Locate every Plasmodium ovale-infected red blood cell.
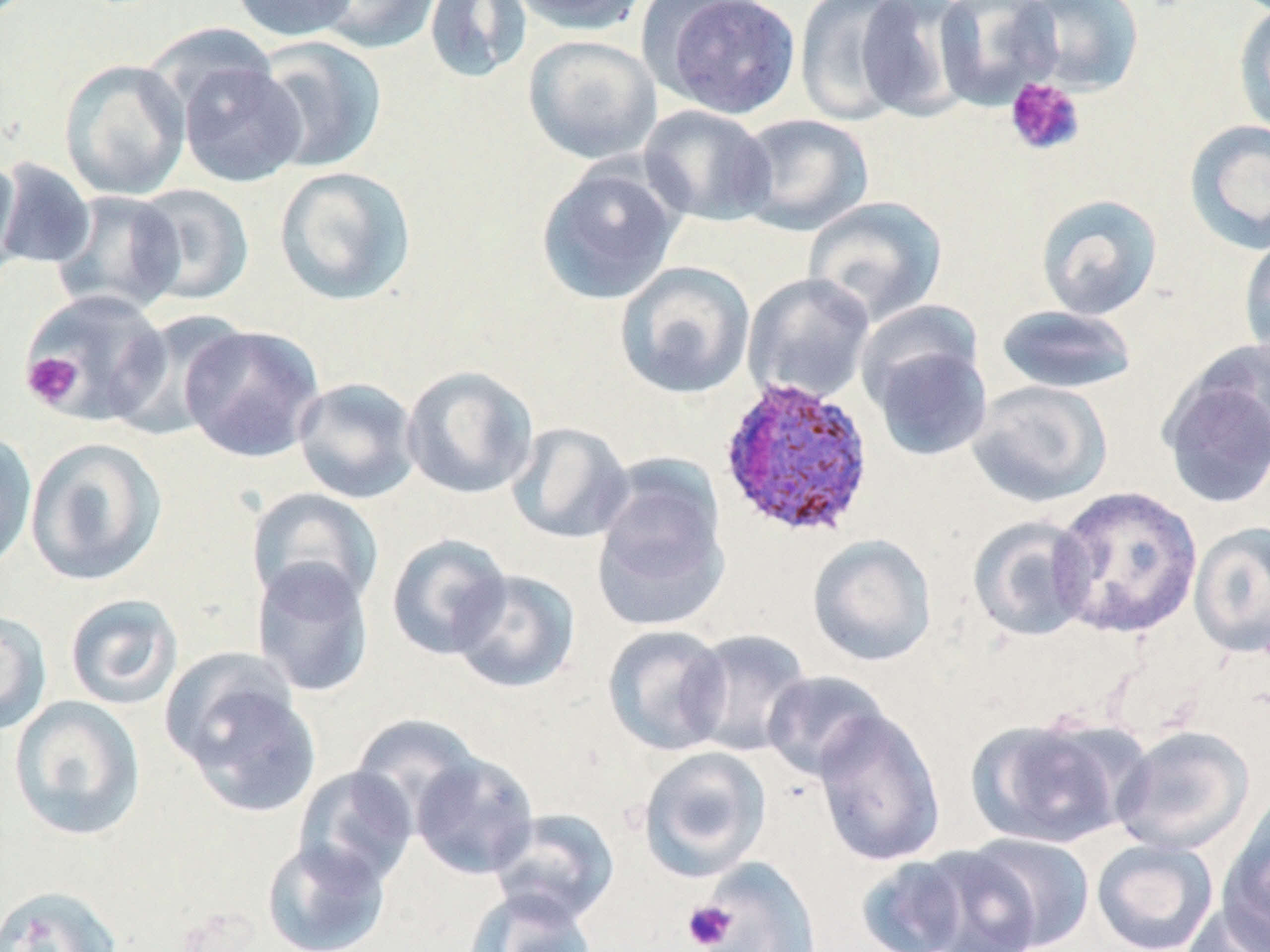

Approximate bounding boxes as (x1, y1, x2, y2) in pixels.
Plasmodium ovale-infected red blood cells: (718, 375, 876, 541).

{
  "slide_level_diagnosis": "Plasmodium ovale",
  "image_size": "1270×952 pixels",
  "preparation": "thin blood smear",
  "platelet_locations": "approximate bounding boxes as (x1, y1, x2, y2) in pixels: (1004, 77, 1086, 157), (22, 351, 83, 409), (682, 900, 737, 950)",
  "magnification": "1000x",
  "stain": "May-Grünwald-Giemsa",
  "modality": "light microscopy",
  "field_of_view": "one of a larger specimen",
  "uninfected_red_blood_cell_locations": "approximate bounding boxes as (x1, y1, x2, y2) in pixels: (230, 0, 359, 42), (311, 0, 441, 54), (423, 0, 532, 84), (507, 0, 650, 34), (649, 0, 802, 119), (794, 0, 920, 126), (854, 0, 974, 121), (933, 0, 1063, 109), (1016, 0, 1144, 95), (1232, 2, 1270, 139), (523, 34, 662, 164), (251, 36, 387, 174), (173, 52, 308, 189), (58, 58, 191, 201), (638, 104, 776, 227), (733, 114, 875, 236), (1183, 119, 1270, 255), (0, 158, 97, 270), (0, 159, 23, 285), (536, 161, 683, 306), (273, 165, 418, 306), (130, 183, 255, 306), (49, 190, 186, 316), (1035, 193, 1163, 320), (802, 196, 948, 327), (1238, 232, 1270, 363), (614, 261, 756, 400), (742, 272, 876, 406), (20, 289, 172, 426), (854, 299, 985, 412), (994, 304, 1139, 395), (109, 310, 252, 441), (179, 324, 325, 463), (868, 339, 993, 461), (1158, 353, 1270, 511), (401, 365, 540, 499), (292, 377, 422, 504), (967, 380, 1113, 508), (506, 421, 635, 544), (0, 429, 37, 574), (25, 436, 167, 587), (590, 459, 732, 631), (1051, 485, 1203, 639), (246, 487, 383, 612), (966, 515, 1097, 642), (1188, 520, 1270, 658), (386, 533, 512, 661), (807, 533, 937, 667), (251, 560, 375, 698), (449, 569, 581, 694), (64, 593, 183, 710), (0, 609, 52, 735), (602, 624, 732, 756), (681, 628, 812, 757), (165, 657, 320, 817), (761, 670, 890, 781), (7, 696, 146, 842), (812, 707, 946, 867), (350, 715, 482, 829), (967, 715, 1130, 849), (1112, 725, 1255, 857), (638, 746, 772, 882), (410, 752, 540, 880), (292, 766, 418, 891), (1219, 796, 1270, 947), (488, 808, 620, 926), (963, 833, 1096, 951), (261, 838, 391, 952), (1091, 838, 1219, 951), (902, 844, 1045, 952), (853, 851, 992, 952), (693, 856, 822, 952), (0, 884, 123, 952), (463, 889, 598, 952), (1179, 902, 1270, 952)"
}